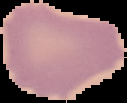
Image is 127×103 pixels. Result: no malaria parasites detected. From a thin blood smear. Segmented cell region on a black background.